Report the malaria status of this cell.
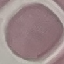
Uninfected.

Giemsa-stained preparation. Acquired by smartphone through the microscope eyepiece. Cell patch, automatically extracted from a larger field of view and resized to 64 × 64 pixels. Thin blood film.